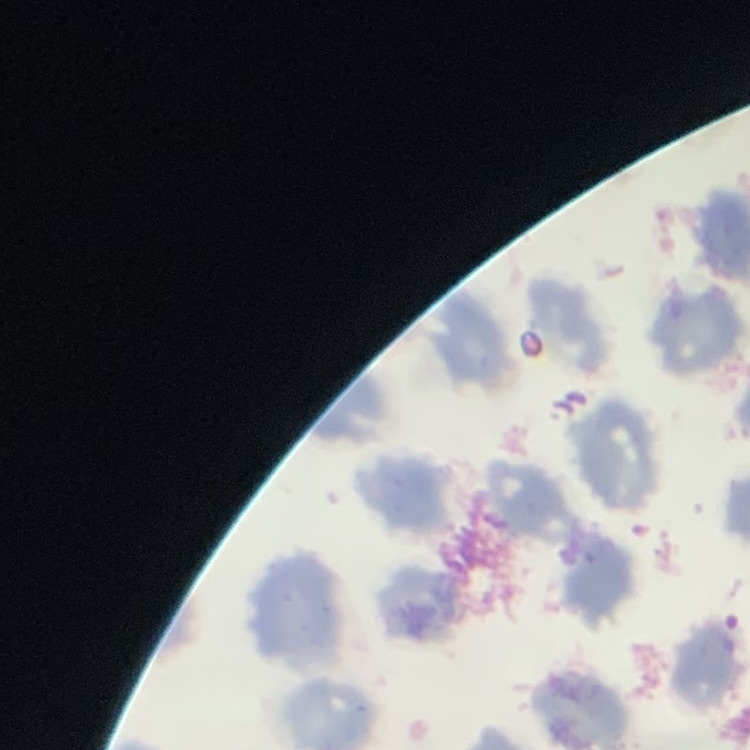
Summary:
  - Red blood cell morphology: no rouleaux formation
  - Preparation: thin blood smear
  - Stain: Field's or Giemsa
  - Image type: square crop of a larger photomicrograph